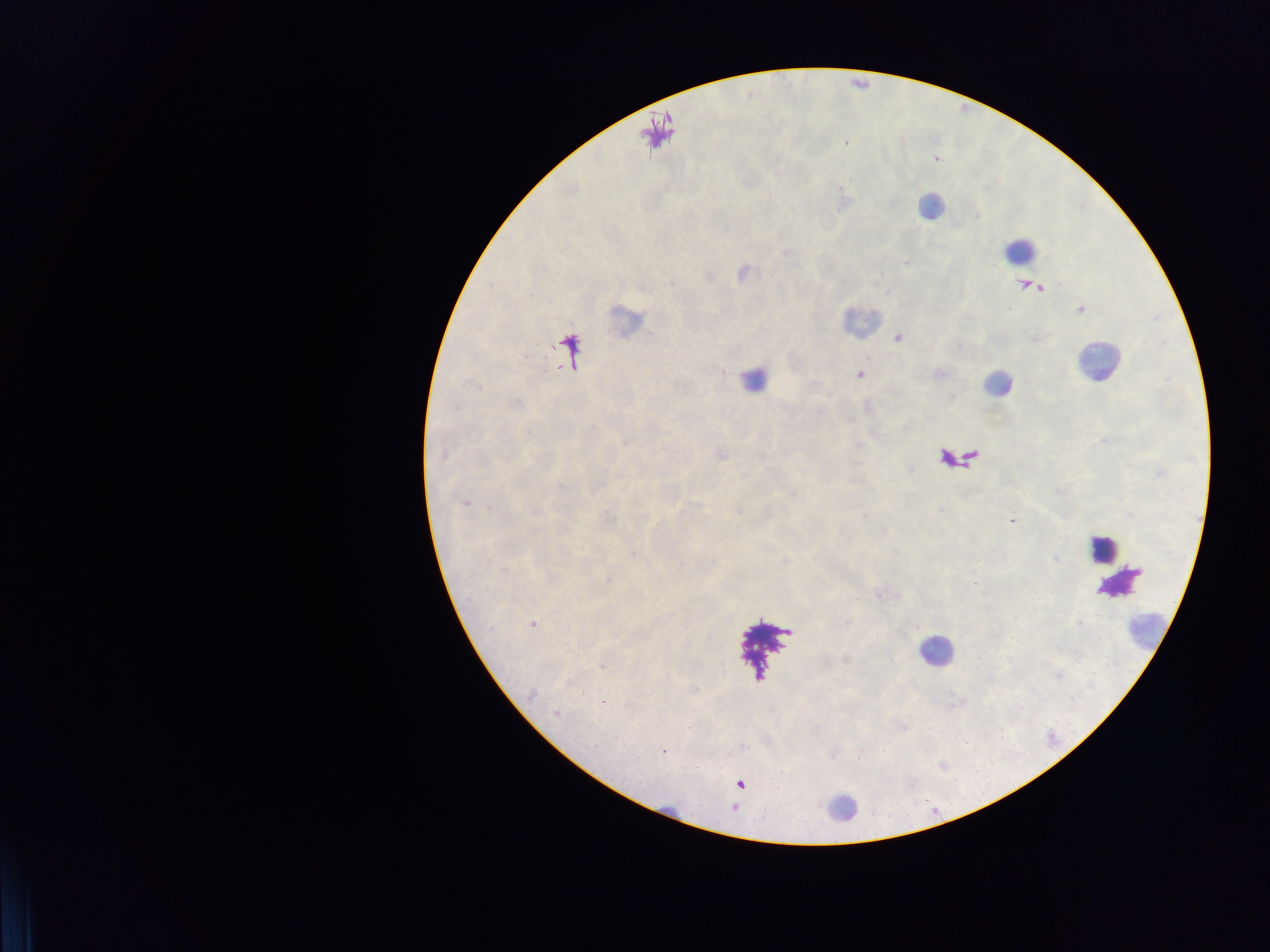
field_of_view: single
capture: mobile-phone photograph through a microscope
image_size: 1270×952 pixels
plasmodium_parasite_locations: 'approximate centers as [x, y] in pixels: [742, 274], [1029, 285], [1080, 309], [898, 337], [859, 373], [442, 454], [720, 454], [464, 503], [1012, 519], [632, 552], [533, 624], [663, 750]'
country: Ghana
leukocyte_locations: 'approximate centers as [x, y] in pixels: [930, 205], [1020, 250], [626, 320], [859, 321], [1099, 362], [753, 379], [997, 384], [1102, 547], [1109, 562], [1119, 581], [1145, 630], [934, 652], [840, 808]'
preparation: thick blood smear